Locate and identify every blood parasite.
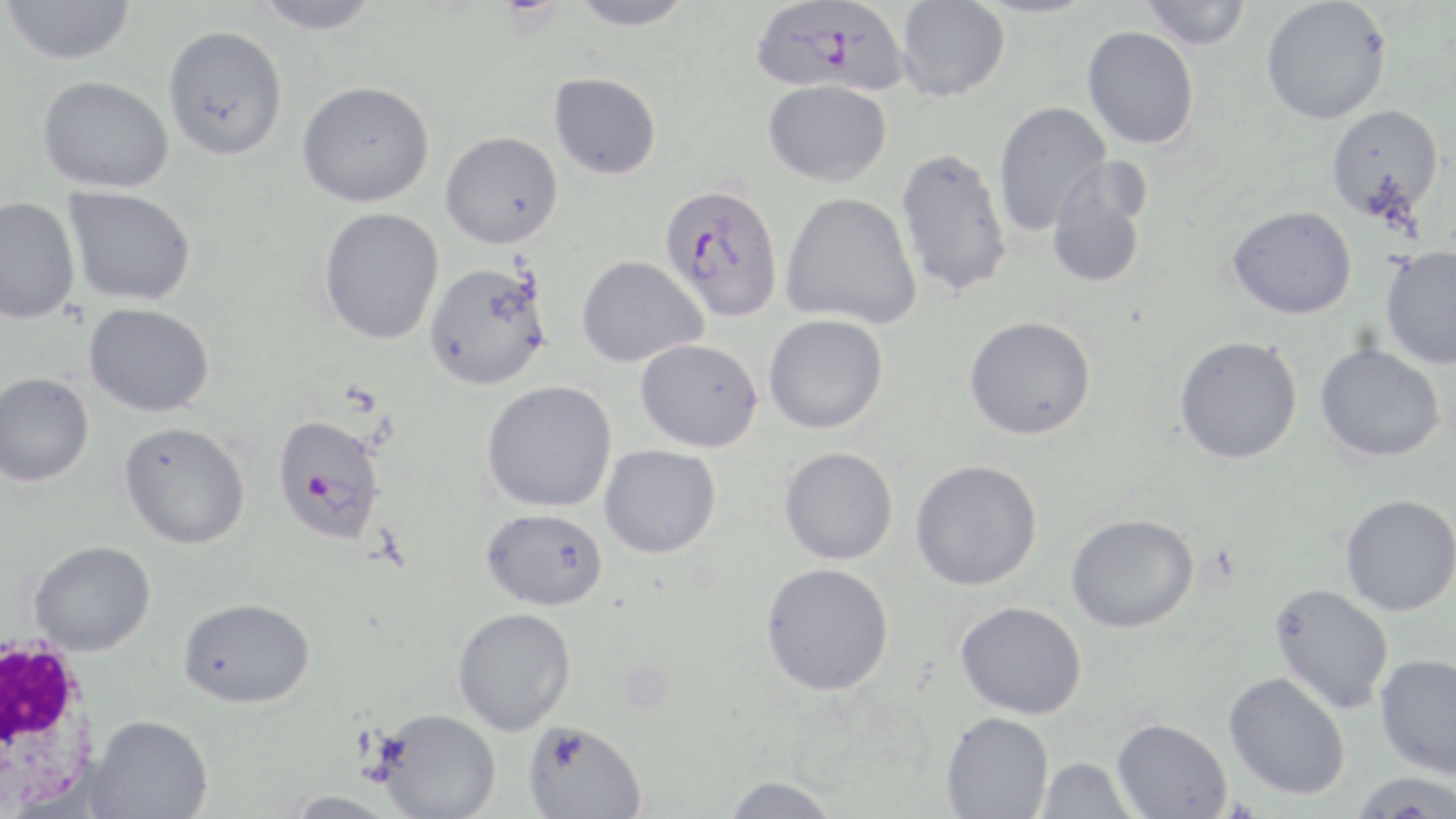
Approximate bounding boxes as named x1/y1/x2/y2 corners in pixels.
Plasmodium falciparum-infected red blood cells: (x1=750, y1=0, x2=910, y2=95), (x1=660, y1=183, x2=784, y2=322), (x1=271, y1=414, x2=387, y2=545).
No Plasmodium ovale, Plasmodium malariae, Plasmodium vivax, Babesia divergens, or Trypanosoma brucei observed.

Summary:
  - Uninfected red blood cell locations: (x1=2, y1=0, x2=136, y2=65), (x1=252, y1=0, x2=382, y2=35), (x1=568, y1=0, x2=698, y2=30), (x1=896, y1=0, x2=1010, y2=101), (x1=1139, y1=0, x2=1251, y2=50), (x1=1261, y1=0, x2=1391, y2=124), (x1=163, y1=25, x2=288, y2=161), (x1=1081, y1=25, x2=1199, y2=149), (x1=549, y1=72, x2=662, y2=180), (x1=37, y1=75, x2=173, y2=193), (x1=763, y1=79, x2=892, y2=187), (x1=297, y1=80, x2=434, y2=207), (x1=993, y1=101, x2=1111, y2=236), (x1=1325, y1=104, x2=1444, y2=223), (x1=440, y1=131, x2=563, y2=248), (x1=896, y1=147, x2=1013, y2=299), (x1=1046, y1=157, x2=1152, y2=290), (x1=63, y1=185, x2=196, y2=305), (x1=780, y1=192, x2=921, y2=328), (x1=0, y1=196, x2=80, y2=324), (x1=1227, y1=205, x2=1357, y2=319), (x1=318, y1=207, x2=444, y2=345), (x1=1380, y1=246, x2=1456, y2=369), (x1=576, y1=255, x2=707, y2=368), (x1=423, y1=261, x2=551, y2=390), (x1=83, y1=302, x2=215, y2=417), (x1=764, y1=314, x2=888, y2=434), (x1=964, y1=316, x2=1097, y2=440), (x1=1175, y1=335, x2=1303, y2=464), (x1=635, y1=338, x2=763, y2=452), (x1=1315, y1=343, x2=1445, y2=462), (x1=0, y1=372, x2=94, y2=487), (x1=482, y1=380, x2=617, y2=513), (x1=119, y1=421, x2=251, y2=549), (x1=599, y1=444, x2=722, y2=559), (x1=779, y1=446, x2=898, y2=565), (x1=911, y1=459, x2=1043, y2=591), (x1=1340, y1=494, x2=1456, y2=616), (x1=482, y1=508, x2=609, y2=611), (x1=1066, y1=513, x2=1199, y2=633), (x1=28, y1=540, x2=155, y2=655), (x1=760, y1=562, x2=894, y2=696), (x1=1270, y1=583, x2=1394, y2=713), (x1=178, y1=597, x2=315, y2=708), (x1=955, y1=600, x2=1087, y2=719), (x1=452, y1=607, x2=576, y2=736), (x1=1375, y1=653, x2=1456, y2=780), (x1=1224, y1=671, x2=1350, y2=800), (x1=376, y1=708, x2=501, y2=818), (x1=941, y1=711, x2=1054, y2=818), (x1=86, y1=715, x2=214, y2=819), (x1=1112, y1=717, x2=1232, y2=819), (x1=523, y1=720, x2=649, y2=819), (x1=1036, y1=757, x2=1137, y2=819), (x1=1349, y1=771, x2=1456, y2=818), (x1=721, y1=776, x2=841, y2=818), (x1=281, y1=790, x2=401, y2=819)
  - White blood cell locations: (x1=0, y1=633, x2=104, y2=817)
  - Slide-level diagnosis: Plasmodium falciparum
  - Stain: May-Grünwald-Giemsa
  - Image size: 1456×819 pixels
  - Magnification: 1000x
  - Field of view: single
  - Preparation: thin blood smear
  - Modality: optical microscopy